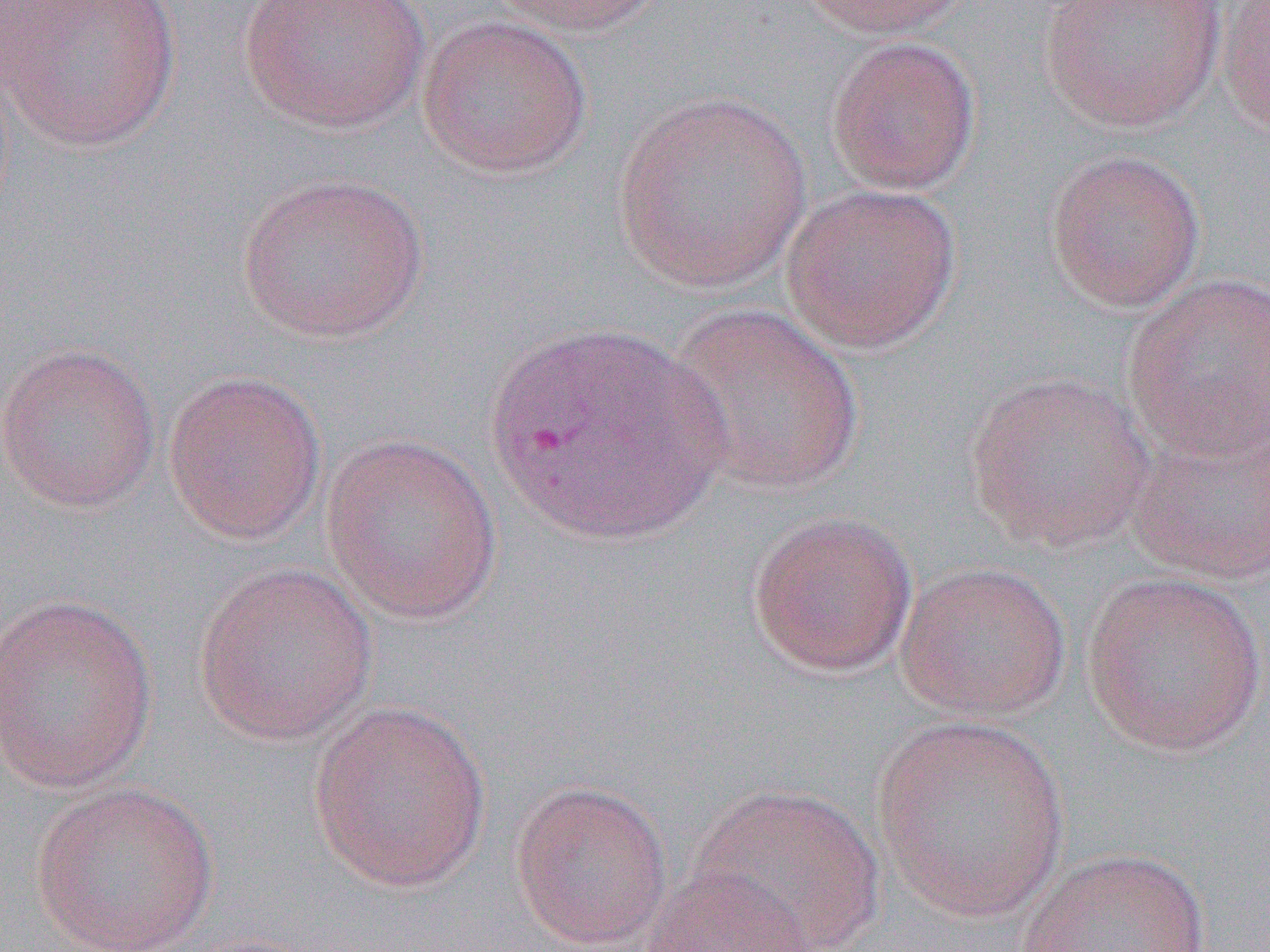
slide_level_diagnosis: Plasmodium vivax
preparation: thin blood smear
plasmodium_vivax_infected_red_blood_cell_locations: 'approximate bounding boxes as [x1, y1, x2, y2] in pixels: [479, 319, 737, 550]'
uninfected_red_blood_cell_locations: 'approximate bounding boxes as [x1, y1, x2, y2] in pixels: [237, 0, 431, 134], [485, 0, 670, 37], [792, 0, 980, 39], [1038, 0, 1228, 133], [1216, 0, 1270, 143], [2, 1, 182, 153], [417, 14, 593, 179], [825, 36, 982, 196], [612, 90, 812, 293], [1043, 147, 1206, 314], [235, 172, 430, 344], [779, 182, 963, 355], [1121, 273, 1270, 462], [663, 301, 866, 499], [0, 342, 162, 512], [162, 369, 328, 545], [963, 370, 1157, 553], [1124, 411, 1270, 585], [320, 432, 504, 624], [746, 509, 919, 678], [193, 561, 378, 745], [894, 562, 1071, 721], [1079, 570, 1267, 756], [0, 591, 158, 792], [305, 698, 492, 893], [870, 715, 1070, 923], [508, 779, 674, 950], [29, 780, 221, 951], [686, 781, 887, 952], [1015, 847, 1212, 952], [641, 867, 818, 952]'
field_of_view: single
magnification: 1000x
modality: light microscopy
image_size: 1270×952 pixels